Classify this cell by malaria status.
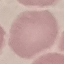
It is uninfected.

Summary:
  - Preparation: thin blood film
  - Image type: cell patch, automatically extracted from a larger field of view and resized to 64 × 64 pixels
  - Capture: smartphone camera at the microscope eyepiece
  - Stain: Giemsa